Report the malaria status of this cell.
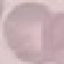

Uninfected.

Summary:
  - Capture: smartphone through the microscope eyepiece
  - Stain: Giemsa
  - Image type: automatically extracted cell patch, resized to 64 × 64 pixels
  - Preparation: thin blood film